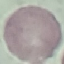
result = negative for malaria parasites
stain = Giemsa
preparation = thin smear
capture = smartphone through the microscope eyepiece
image type = automatically extracted cell patch, resized to 64 × 64 pixels